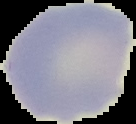
{
  "result": "negative for malaria parasites",
  "preparation": "thin blood smear",
  "image_size": "136×124 pixels",
  "image_type": "segmented cell region with the area outside set to black"
}